Assess the morphology of the red blood cells.
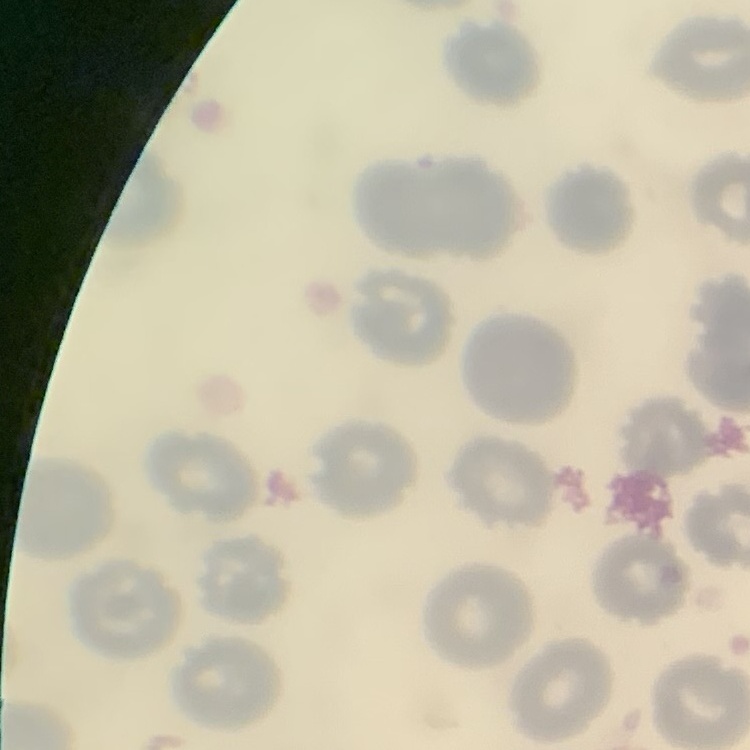

No rouleaux formation.

{
  "stain": "Field's or Giemsa",
  "preparation": "thin peripheral smear",
  "image_type": "one tile cut from a larger photomicrograph"
}